Report the malaria status of this cell.
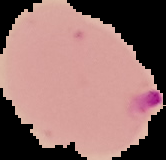
Parasitized.

Image is 166×160 pixels. Segmented cell region on a black background. From a thin blood smear.